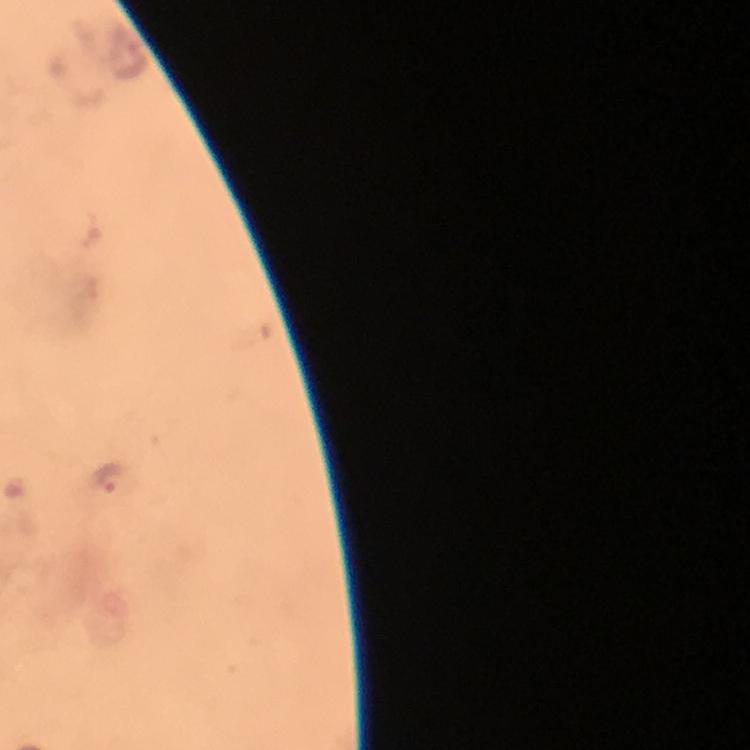
Approximate centers as {x, y} in pixels. Malaria parasite locations: {111, 480}. From a diagnostic examination for malaria. Immersion oil applied. A crop from one field of view. Giemsa stain. At 100x magnification. Image is 750×750 pixels. Thick blood film. Photographed through the microscope with a smartphone camera.